Assess the morphology of the erythrocytes.
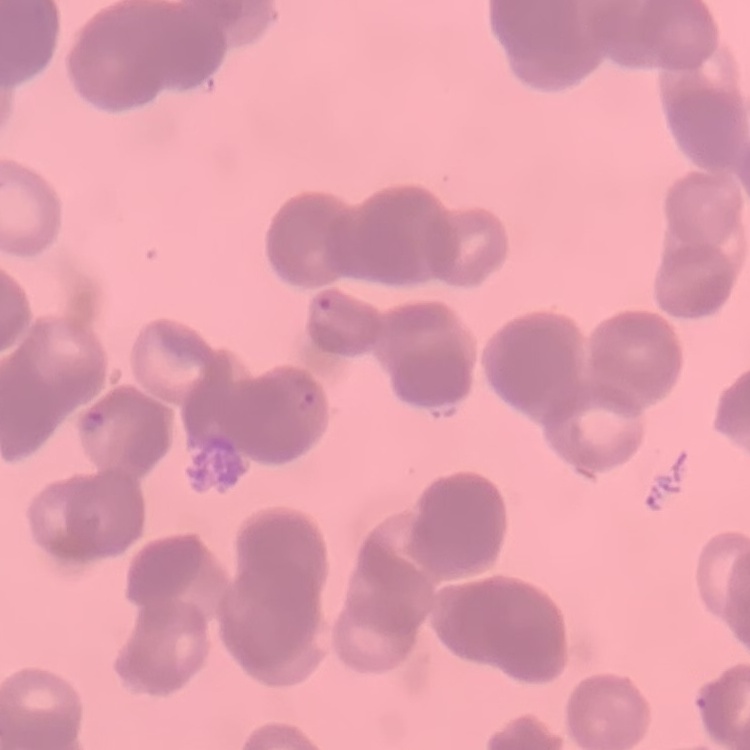
Rouleaux formation.

Summary:
  - Image type: one tile cut from a larger photomicrograph
  - Stain: Field's or Giemsa
  - Preparation: thin blood film